Classify this cell by malaria status.
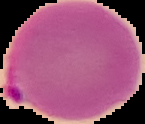
Parasitized.

preparation = thin blood smear
image size = 145×124 pixels
image type = cell region segmented out of the field of view; surrounding area masked to black